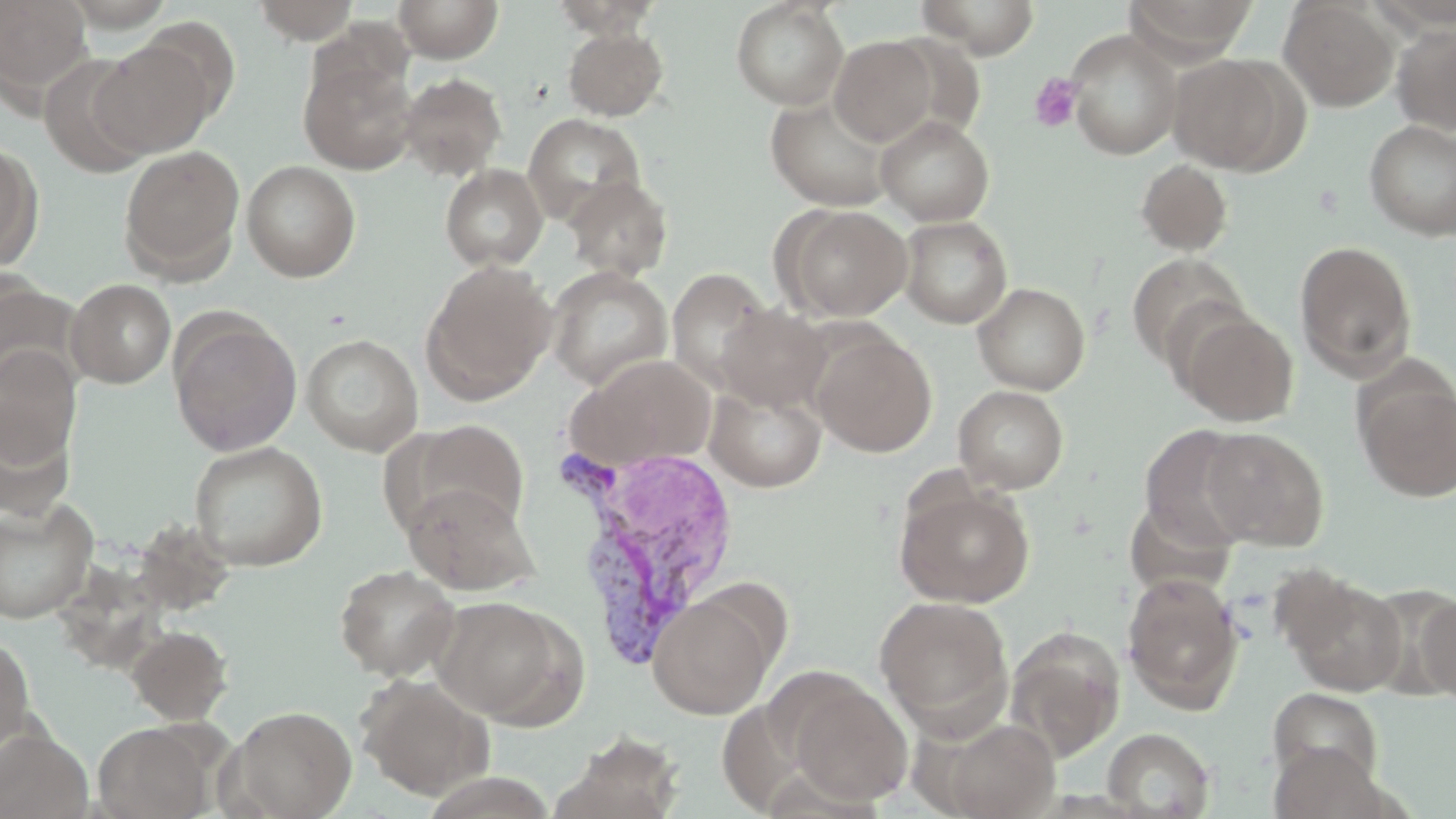
Approximate bounding boxes as named x1/y1/x2/y2 corners in pixels. Uninfected red blood cell locations: (x1=0, y1=0, x2=94, y2=100), (x1=247, y1=0, x2=366, y2=43), (x1=393, y1=0, x2=504, y2=62), (x1=546, y1=0, x2=665, y2=38), (x1=913, y1=0, x2=1041, y2=57), (x1=1124, y1=0, x2=1259, y2=61), (x1=730, y1=1, x2=849, y2=109), (x1=1279, y1=1, x2=1398, y2=111), (x1=136, y1=17, x2=242, y2=127), (x1=1392, y1=23, x2=1456, y2=136), (x1=562, y1=26, x2=669, y2=121), (x1=1065, y1=29, x2=1183, y2=160), (x1=829, y1=35, x2=940, y2=147), (x1=91, y1=37, x2=220, y2=157), (x1=299, y1=50, x2=418, y2=175), (x1=39, y1=54, x2=155, y2=176), (x1=1168, y1=54, x2=1299, y2=173), (x1=397, y1=73, x2=508, y2=181), (x1=765, y1=95, x2=895, y2=211), (x1=523, y1=113, x2=646, y2=225), (x1=876, y1=115, x2=994, y2=225), (x1=1364, y1=120, x2=1456, y2=239), (x1=0, y1=139, x2=42, y2=270), (x1=119, y1=144, x2=244, y2=280), (x1=241, y1=159, x2=361, y2=282), (x1=1136, y1=159, x2=1233, y2=256), (x1=440, y1=164, x2=548, y2=270), (x1=564, y1=175, x2=674, y2=281), (x1=781, y1=204, x2=912, y2=321), (x1=899, y1=215, x2=1012, y2=328), (x1=1294, y1=240, x2=1418, y2=380), (x1=1126, y1=251, x2=1252, y2=368), (x1=421, y1=259, x2=556, y2=403), (x1=545, y1=266, x2=673, y2=390), (x1=667, y1=267, x2=775, y2=391), (x1=0, y1=277, x2=83, y2=394), (x1=66, y1=279, x2=176, y2=388), (x1=972, y1=282, x2=1090, y2=394), (x1=716, y1=304, x2=831, y2=411), (x1=1176, y1=308, x2=1299, y2=426), (x1=168, y1=314, x2=303, y2=456), (x1=810, y1=331, x2=937, y2=456), (x1=301, y1=333, x2=423, y2=456), (x1=0, y1=346, x2=82, y2=469), (x1=569, y1=354, x2=717, y2=470), (x1=1356, y1=375, x2=1456, y2=502), (x1=705, y1=380, x2=828, y2=493), (x1=953, y1=385, x2=1069, y2=493), (x1=0, y1=402, x2=76, y2=520), (x1=411, y1=420, x2=529, y2=533), (x1=1136, y1=426, x2=1256, y2=552), (x1=1199, y1=426, x2=1329, y2=550), (x1=188, y1=441, x2=328, y2=571), (x1=402, y1=482, x2=538, y2=596), (x1=894, y1=483, x2=1034, y2=607), (x1=0, y1=496, x2=99, y2=623), (x1=334, y1=564, x2=461, y2=681), (x1=1122, y1=572, x2=1245, y2=715), (x1=1283, y1=573, x2=1408, y2=697), (x1=647, y1=589, x2=777, y2=719), (x1=1416, y1=591, x2=1456, y2=706), (x1=432, y1=595, x2=580, y2=726), (x1=874, y1=596, x2=1013, y2=730), (x1=1003, y1=624, x2=1126, y2=761), (x1=126, y1=625, x2=234, y2=725), (x1=0, y1=635, x2=35, y2=756), (x1=356, y1=674, x2=494, y2=800), (x1=786, y1=678, x2=912, y2=806), (x1=1266, y1=686, x2=1385, y2=792), (x1=225, y1=705, x2=357, y2=818), (x1=931, y1=716, x2=1061, y2=819), (x1=93, y1=722, x2=211, y2=819), (x1=1102, y1=727, x2=1215, y2=818), (x1=0, y1=728, x2=93, y2=818), (x1=552, y1=731, x2=686, y2=819). Platelet locations: (x1=1028, y1=72, x2=1084, y2=133). Plasmodium vivax-infected red blood cell locations: (x1=554, y1=440, x2=742, y2=668). Slide-level diagnosis: Plasmodium vivax. 1000x magnification. Light microscopy. May-Grünwald-Giemsa stain. Image is 1456×819 pixels. Thin blood film. One field of a larger specimen.